Name the parasite shown.
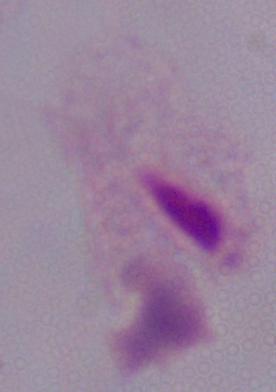

This is a trichomonad.

Captured at 1000x magnification. Photomicrograph.